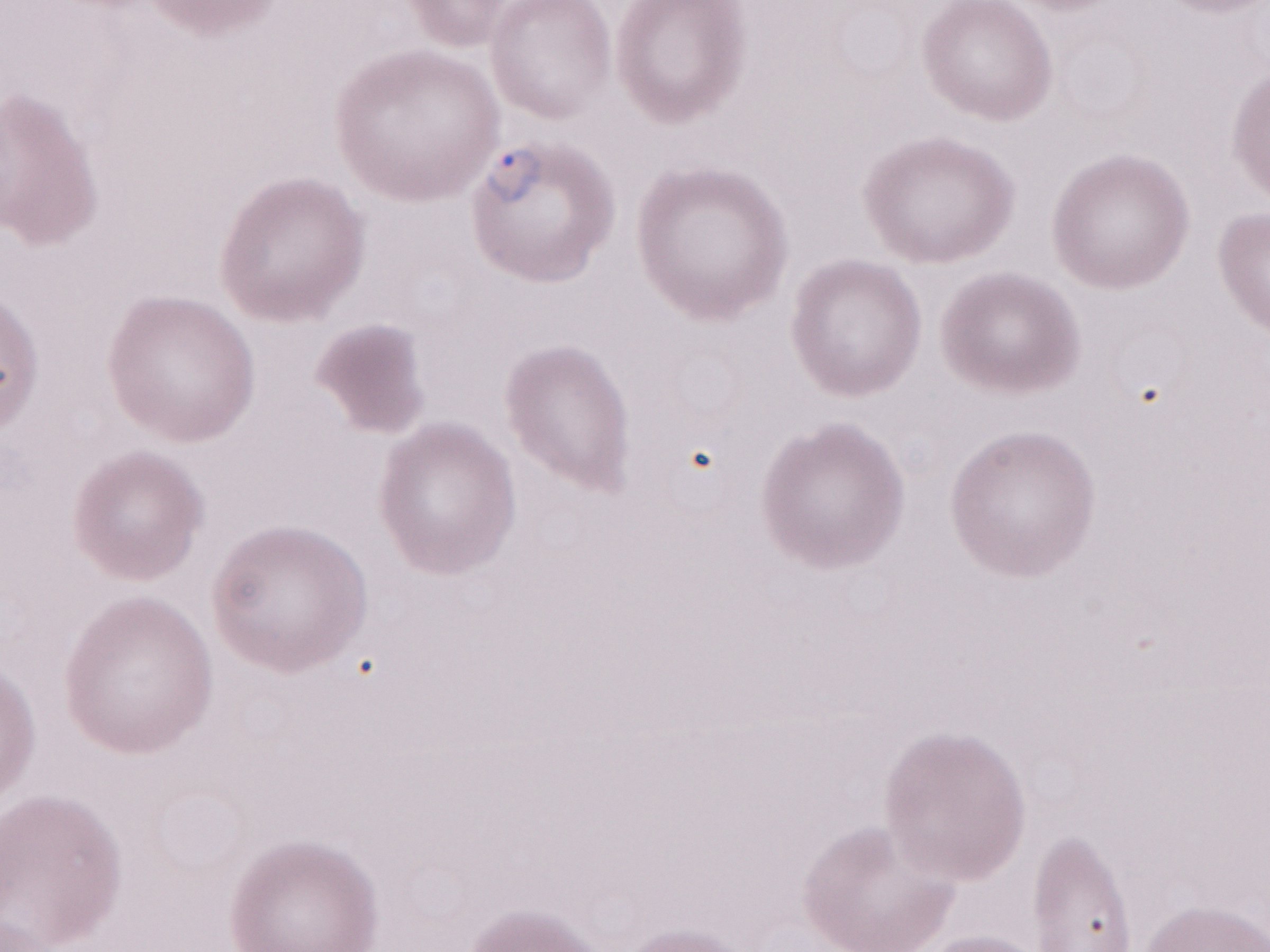
Thin blood film. Magnification: 1,000x. Single field of view. Patient diagnosis: malaria infection. Olympus BX43 microscope, Olympus DP73 camera. May-Grünwald-Giemsa stain. Image is 1270×952 pixels.